Name the cell type shown.
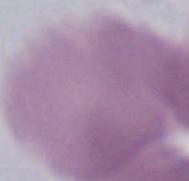

An erythrocyte.

Captured at 1000x magnification. Photomicrograph.